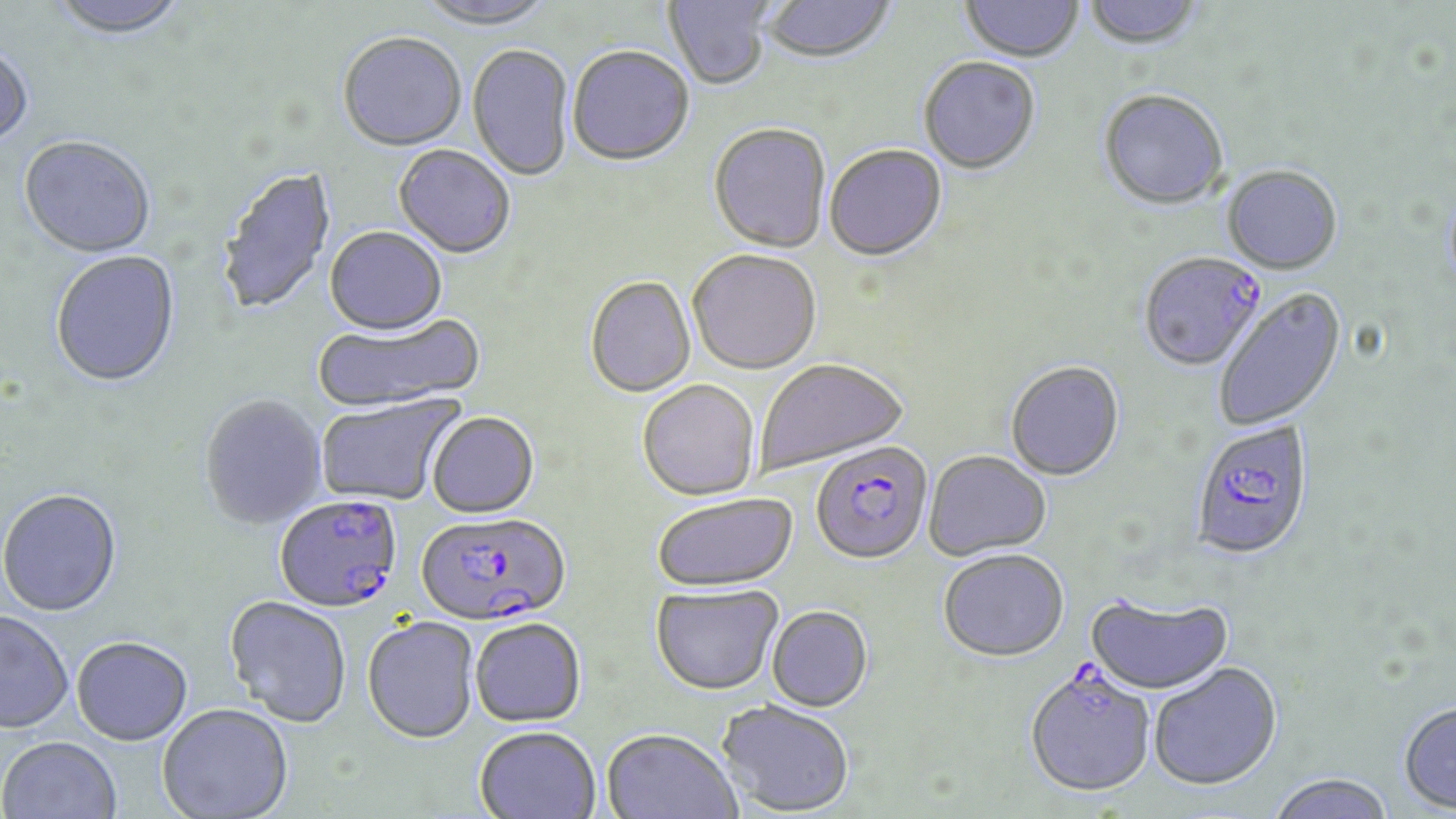
Approximate bounding boxes as named x1/y1/x2/y2 corners in pixels. Plasmodium falciparum-infected red blood cell locations: (x1=1138, y1=254, x2=1267, y2=374), (x1=1190, y1=421, x2=1315, y2=563), (x1=810, y1=442, x2=934, y2=567), (x1=275, y1=497, x2=402, y2=616), (x1=416, y1=514, x2=572, y2=627), (x1=1024, y1=670, x2=1156, y2=799). Uninfected red blood cell locations: (x1=47, y1=0, x2=190, y2=43), (x1=664, y1=0, x2=773, y2=92), (x1=761, y1=0, x2=896, y2=67), (x1=1083, y1=0, x2=1203, y2=53), (x1=416, y1=1, x2=558, y2=32), (x1=959, y1=1, x2=1083, y2=65), (x1=337, y1=35, x2=467, y2=154), (x1=467, y1=46, x2=574, y2=182), (x1=0, y1=48, x2=34, y2=154), (x1=567, y1=49, x2=694, y2=169), (x1=918, y1=58, x2=1041, y2=176), (x1=1097, y1=92, x2=1229, y2=213), (x1=708, y1=125, x2=831, y2=255), (x1=18, y1=138, x2=156, y2=260), (x1=824, y1=145, x2=948, y2=264), (x1=393, y1=146, x2=515, y2=260), (x1=216, y1=167, x2=337, y2=318), (x1=1222, y1=167, x2=1342, y2=276), (x1=324, y1=228, x2=448, y2=338), (x1=50, y1=252, x2=181, y2=390), (x1=688, y1=252, x2=821, y2=377), (x1=585, y1=278, x2=696, y2=398), (x1=1213, y1=288, x2=1347, y2=432), (x1=312, y1=314, x2=486, y2=415), (x1=755, y1=360, x2=909, y2=476), (x1=1005, y1=362, x2=1125, y2=483), (x1=637, y1=381, x2=760, y2=502), (x1=316, y1=393, x2=466, y2=507), (x1=199, y1=396, x2=329, y2=530), (x1=426, y1=413, x2=539, y2=520), (x1=924, y1=452, x2=1051, y2=562), (x1=0, y1=491, x2=122, y2=619), (x1=653, y1=495, x2=798, y2=593), (x1=938, y1=551, x2=1069, y2=664), (x1=650, y1=585, x2=783, y2=696), (x1=1085, y1=593, x2=1234, y2=696), (x1=223, y1=598, x2=352, y2=729), (x1=767, y1=606, x2=873, y2=712), (x1=0, y1=612, x2=73, y2=735), (x1=362, y1=618, x2=480, y2=746), (x1=470, y1=619, x2=587, y2=728), (x1=72, y1=639, x2=193, y2=748), (x1=1148, y1=662, x2=1282, y2=793), (x1=716, y1=699, x2=855, y2=816), (x1=1398, y1=702, x2=1456, y2=813), (x1=157, y1=705, x2=293, y2=819), (x1=474, y1=727, x2=600, y2=819), (x1=601, y1=729, x2=742, y2=819), (x1=1, y1=738, x2=122, y2=819), (x1=1265, y1=773, x2=1396, y2=819). Slide-level diagnosis: Plasmodium falciparum. Image is 1456×819 pixels. Captured at 1000x magnification. Single field of view. Thin blood smear. May-Grünwald-Giemsa stain. Optical microscopy.